Assess this cell for malaria.
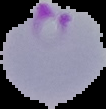

Parasitized.

preparation = thin blood smear
image type = cell region segmented out of the field of view; surrounding area masked to black
image size = 106×109 pixels